Give the extent of all Plasmodium falciparum-infected red blood cells.
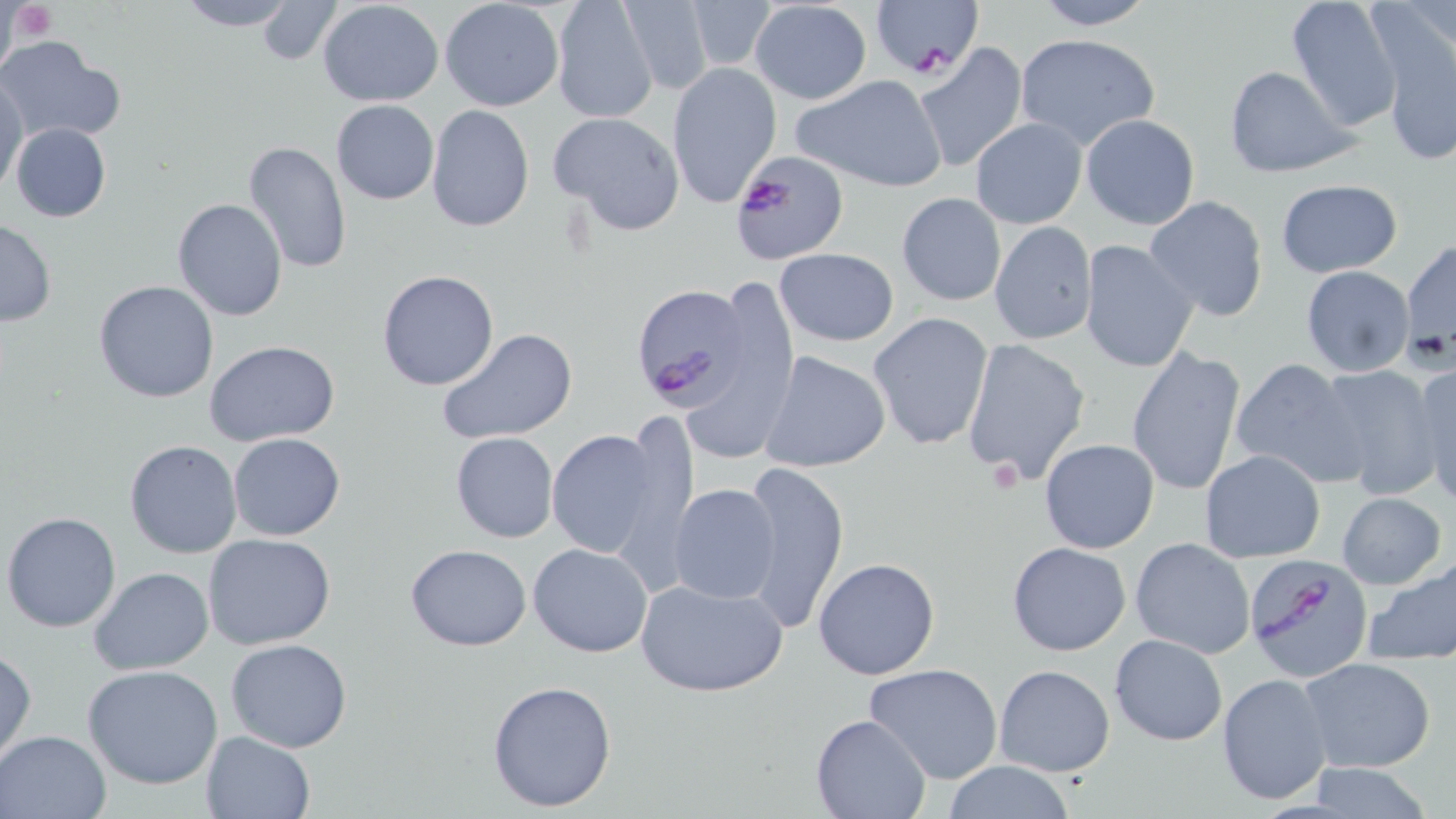
Approximate bounding boxes as [x1, y1, x2, y2] in pixels.
Plasmodium falciparum-infected red blood cells: [872, 2, 981, 81], [730, 149, 848, 266], [631, 284, 753, 409], [1243, 551, 1376, 680].

Platelet locations: [9, 2, 56, 42], [988, 457, 1024, 494]. Uninfected red blood cell locations: [173, 0, 298, 31], [256, 0, 341, 65], [550, 0, 659, 125], [616, 0, 716, 95], [1032, 0, 1157, 30], [1284, 0, 1404, 130], [317, 1, 444, 107], [439, 1, 565, 112], [681, 1, 782, 73], [748, 1, 872, 104], [1375, 20, 1456, 167], [1013, 33, 1163, 152], [0, 38, 125, 144], [912, 42, 1028, 175], [666, 63, 782, 208], [1222, 64, 1357, 178], [793, 72, 949, 194], [0, 75, 27, 196], [330, 100, 439, 205], [426, 104, 534, 233], [548, 110, 686, 236], [1079, 114, 1199, 228], [968, 119, 1087, 228], [9, 121, 111, 223], [243, 140, 352, 274], [1274, 179, 1403, 277], [897, 192, 1006, 307], [1143, 195, 1271, 322], [171, 197, 288, 321], [932, 201, 1083, 326], [0, 218, 56, 326], [988, 221, 1097, 346], [1400, 237, 1456, 361], [1079, 238, 1199, 374], [774, 248, 899, 346], [1300, 266, 1416, 377], [375, 270, 500, 391], [693, 275, 800, 462], [94, 280, 220, 404], [868, 312, 996, 451], [437, 326, 579, 445], [960, 338, 1092, 485], [205, 341, 340, 449], [1125, 346, 1246, 496], [761, 349, 891, 473], [1227, 358, 1367, 487], [1409, 362, 1456, 503], [1315, 365, 1444, 501], [546, 426, 673, 564], [450, 431, 559, 543], [228, 432, 346, 542], [1039, 438, 1160, 553], [123, 439, 243, 558], [1198, 450, 1326, 562], [738, 460, 849, 636], [669, 484, 781, 605], [1336, 491, 1446, 589], [3, 511, 123, 632], [203, 533, 336, 650], [1129, 537, 1256, 658], [1007, 541, 1131, 656], [527, 542, 654, 658], [405, 543, 532, 651], [813, 557, 941, 681], [1363, 557, 1456, 663], [89, 566, 214, 675], [634, 575, 787, 696], [1109, 633, 1227, 746], [224, 639, 352, 753], [1, 648, 36, 768], [1299, 655, 1437, 774], [865, 663, 1003, 785], [82, 664, 224, 789], [994, 664, 1115, 778], [1215, 673, 1333, 805], [486, 679, 620, 814], [809, 714, 930, 819], [1, 729, 110, 818], [200, 729, 316, 819], [939, 761, 1078, 818], [1303, 763, 1438, 818]. Slide-level diagnosis: Plasmodium falciparum. May-Grünwald-Giemsa-stained preparation. Thin blood film. Captured at 1000x magnification. Single field of view. Image is 1456×819 pixels. Optical microscopy.